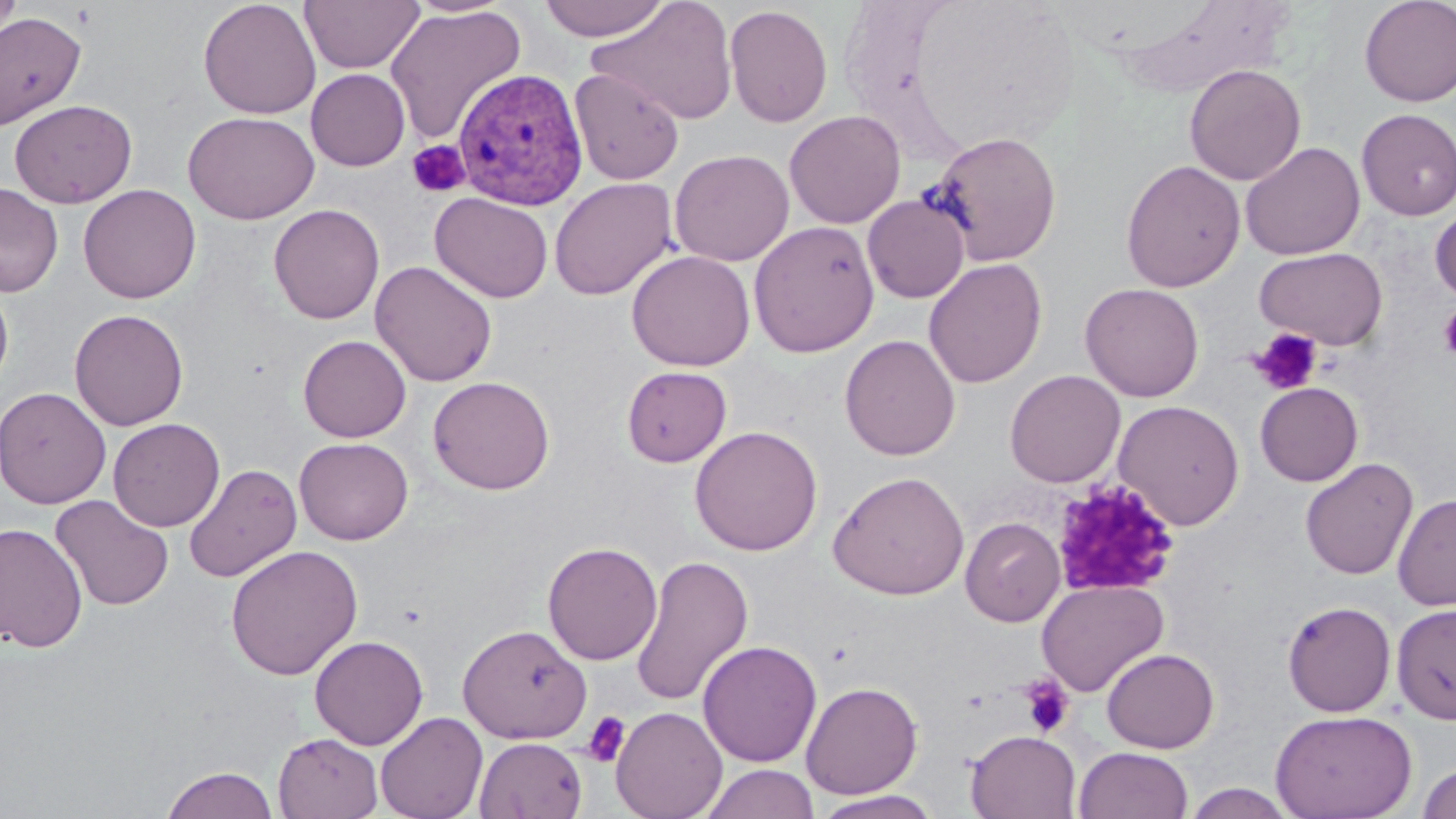

Summary:
  - Coordinate format: approximate bounding boxes as named x1/y1/x2/y2 corners in pixels
  - Plasmodium vivax-infected red blood cell locations: (x1=452, y1=68, x2=589, y2=210)
  - Platelet locations: (x1=406, y1=140, x2=470, y2=198), (x1=1438, y1=304, x2=1456, y2=363), (x1=1249, y1=328, x2=1324, y2=396), (x1=1049, y1=478, x2=1180, y2=599), (x1=1018, y1=675, x2=1076, y2=738), (x1=581, y1=710, x2=631, y2=768)
  - Uninfected red blood cell locations: (x1=0, y1=0, x2=22, y2=49), (x1=198, y1=0, x2=321, y2=119), (x1=300, y1=0, x2=424, y2=73), (x1=536, y1=0, x2=672, y2=42), (x1=587, y1=0, x2=739, y2=126), (x1=1359, y1=0, x2=1456, y2=108), (x1=1113, y1=2, x2=1298, y2=95), (x1=723, y1=4, x2=833, y2=128), (x1=385, y1=6, x2=526, y2=144), (x1=0, y1=11, x2=85, y2=130), (x1=1184, y1=64, x2=1306, y2=185), (x1=306, y1=68, x2=410, y2=171), (x1=571, y1=68, x2=684, y2=186), (x1=8, y1=99, x2=137, y2=208), (x1=1356, y1=108, x2=1456, y2=220), (x1=784, y1=109, x2=906, y2=229), (x1=183, y1=110, x2=320, y2=224), (x1=926, y1=130, x2=1062, y2=266), (x1=1241, y1=142, x2=1365, y2=260), (x1=669, y1=149, x2=794, y2=266), (x1=1120, y1=159, x2=1245, y2=292), (x1=549, y1=177, x2=678, y2=301), (x1=0, y1=181, x2=63, y2=298), (x1=78, y1=184, x2=201, y2=304), (x1=429, y1=191, x2=553, y2=303), (x1=862, y1=194, x2=970, y2=303), (x1=1431, y1=203, x2=1456, y2=306), (x1=268, y1=204, x2=385, y2=324), (x1=748, y1=220, x2=880, y2=358), (x1=1254, y1=246, x2=1388, y2=350), (x1=626, y1=250, x2=755, y2=371), (x1=923, y1=258, x2=1047, y2=388), (x1=370, y1=260, x2=497, y2=387), (x1=0, y1=281, x2=13, y2=396), (x1=1080, y1=282, x2=1205, y2=401), (x1=69, y1=308, x2=189, y2=431), (x1=840, y1=334, x2=961, y2=461), (x1=298, y1=335, x2=411, y2=442), (x1=621, y1=365, x2=732, y2=467), (x1=1004, y1=370, x2=1126, y2=487), (x1=428, y1=375, x2=555, y2=495), (x1=1254, y1=381, x2=1363, y2=486), (x1=0, y1=386, x2=112, y2=508), (x1=1113, y1=399, x2=1245, y2=530), (x1=108, y1=418, x2=225, y2=532), (x1=690, y1=425, x2=823, y2=556), (x1=294, y1=437, x2=413, y2=545), (x1=1300, y1=457, x2=1419, y2=580), (x1=183, y1=464, x2=302, y2=582), (x1=828, y1=470, x2=969, y2=601), (x1=1393, y1=492, x2=1456, y2=612), (x1=50, y1=494, x2=174, y2=611), (x1=960, y1=516, x2=1065, y2=626), (x1=0, y1=522, x2=88, y2=653), (x1=542, y1=540, x2=662, y2=665), (x1=225, y1=544, x2=363, y2=680), (x1=629, y1=555, x2=754, y2=709), (x1=1036, y1=579, x2=1169, y2=697), (x1=1281, y1=599, x2=1397, y2=717), (x1=1392, y1=602, x2=1456, y2=725), (x1=457, y1=623, x2=591, y2=743), (x1=309, y1=635, x2=428, y2=750), (x1=697, y1=640, x2=822, y2=767), (x1=1101, y1=647, x2=1219, y2=753), (x1=800, y1=681, x2=923, y2=799), (x1=611, y1=706, x2=727, y2=819), (x1=1270, y1=709, x2=1417, y2=819), (x1=375, y1=711, x2=488, y2=819), (x1=965, y1=729, x2=1082, y2=819), (x1=273, y1=732, x2=383, y2=819), (x1=474, y1=736, x2=588, y2=819), (x1=1073, y1=746, x2=1194, y2=819), (x1=1417, y1=761, x2=1456, y2=819), (x1=699, y1=763, x2=820, y2=819), (x1=160, y1=766, x2=279, y2=818), (x1=1181, y1=783, x2=1298, y2=818), (x1=811, y1=791, x2=944, y2=819)
  - Slide-level diagnosis: Plasmodium vivax
  - Stain: May-Grünwald-Giemsa
  - Preparation: thin blood film
  - Image size: 1456×819 pixels
  - Modality: light microscopy
  - Field of view: single
  - Magnification: 1000x